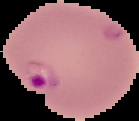
Summary:
  - Image size: 139×121 pixels
  - Preparation: thin blood smear
  - Image type: segmented cell region on a black background
  - Result: malaria parasites identified